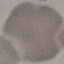

{
  "result": "negative for malaria parasites",
  "preparation": "thin smear",
  "capture": "smartphone through the microscope eyepiece",
  "stain": "Giemsa",
  "image_type": "cell patch, automatically extracted from a larger field of view and resized to 64 × 64 pixels"
}